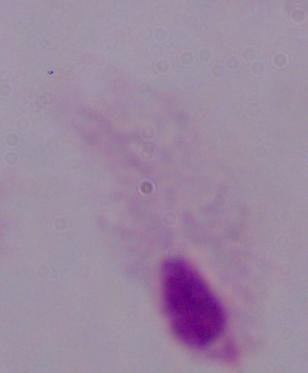
magnification = 1000x
identification = trichomonad
modality = micrograph